Report the malaria status of this cell.
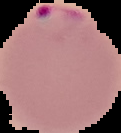

Parasitized.

The area outside the segmented cell region is set to black. Image is 121×133 pixels. From a thin blood smear.